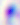
identification = Toxoplasma gondii
modality = micrograph
magnification = 400x